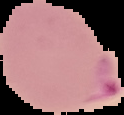 Result: Plasmodium parasites detected. The area outside the segmented cell region is set to black. From a thin blood smear. Image is 124×115 pixels.